Describe the morphology of the red blood cells.
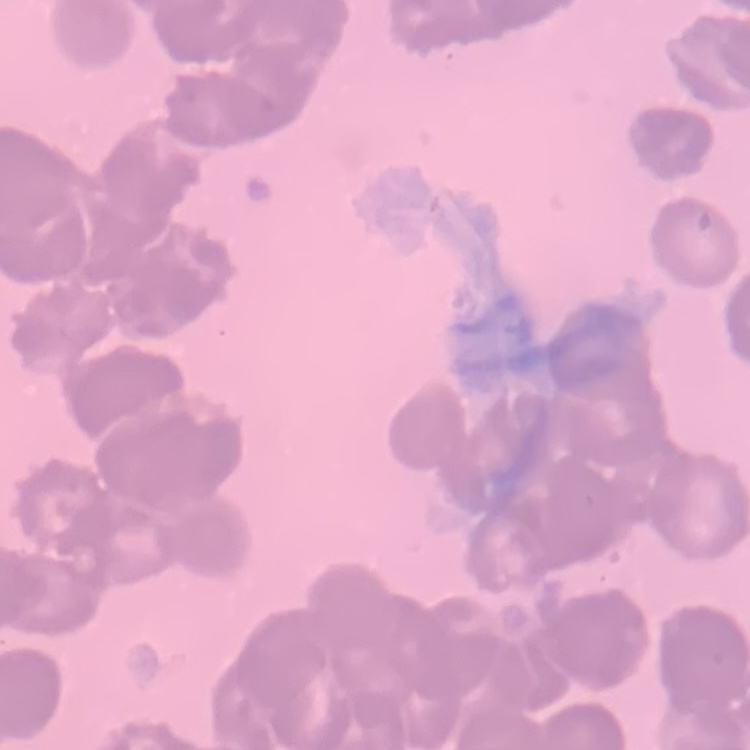

Rouleaux formation.

Summary:
  - Stain: Field's or Giemsa
  - Preparation: thin peripheral smear
  - Image type: square crop of a larger photomicrograph